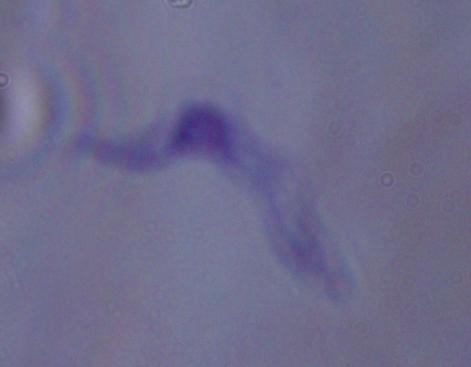

identification = trypanosome
magnification = 1000x
modality = photomicrograph